Classify this cell by malaria status.
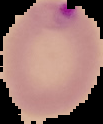

It is parasitized.

Image is 103×124 pixels. From a thin blood smear. Segmented cell region on a black background.